Assess this cell for malaria.
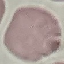
It is uninfected.

Giemsa-stained preparation. Photographed with a smartphone camera at the microscope eyepiece. Automatically extracted cell patch, resized to 64 × 64 pixels. Thin smear of blood.